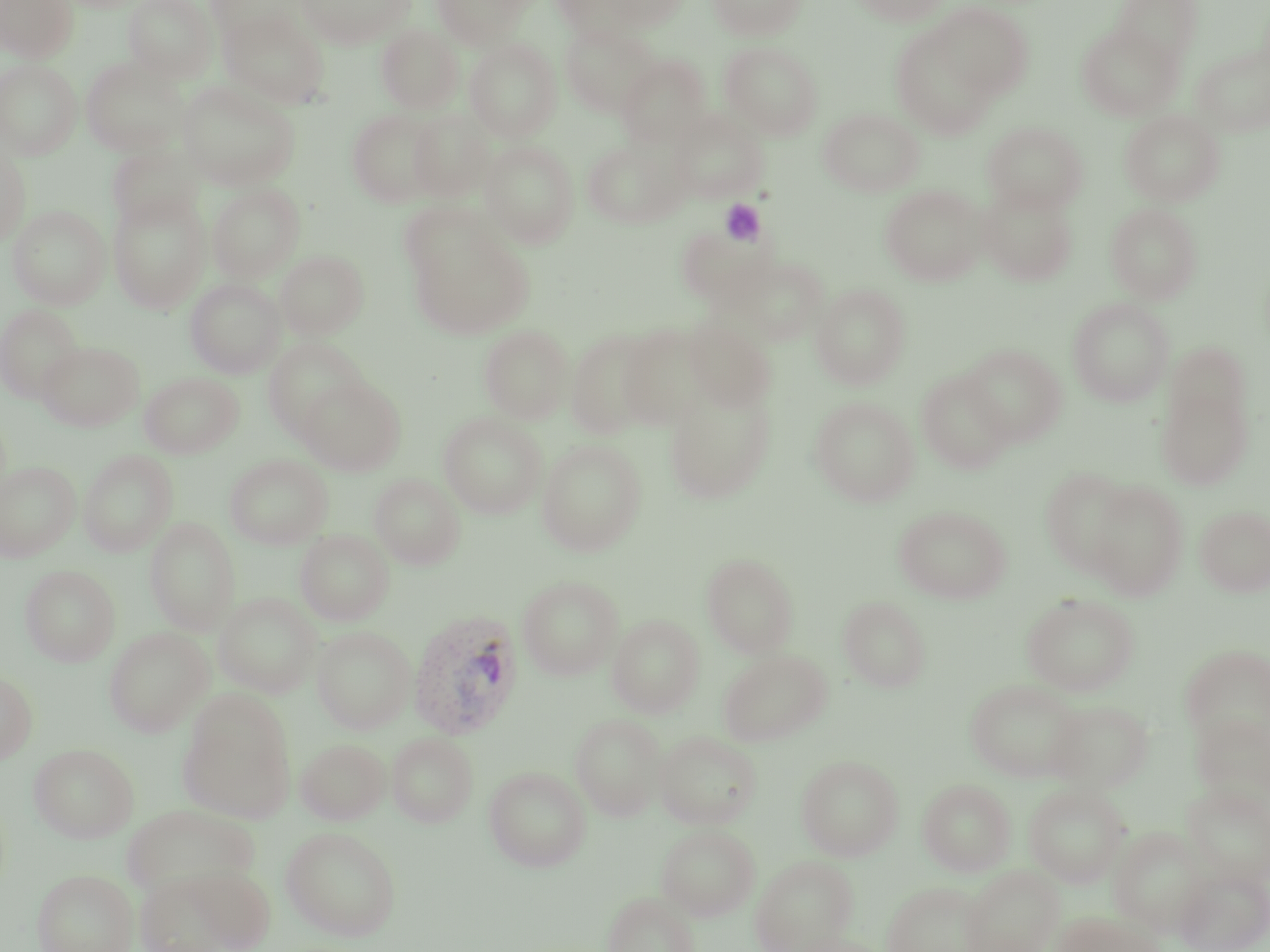
Approximate bounding boxes as [x1, y1, x2, y2] in pixels. Platelet locations: [720, 198, 766, 246]. Uninfected red blood cell locations: [0, 0, 78, 62], [124, 0, 218, 82], [297, 0, 411, 49], [552, 0, 641, 40], [607, 0, 689, 30], [707, 0, 808, 40], [852, 0, 949, 26], [1112, 0, 1202, 68], [206, 1, 306, 46], [430, 1, 530, 47], [931, 2, 1033, 99], [219, 12, 330, 108], [890, 22, 1003, 140], [561, 23, 660, 116], [376, 24, 463, 114], [1076, 24, 1183, 120], [464, 38, 562, 142], [720, 41, 823, 140], [1192, 43, 1270, 138], [617, 55, 710, 147], [81, 57, 188, 156], [0, 58, 82, 159], [177, 80, 300, 190], [819, 108, 923, 197], [346, 109, 443, 207], [1119, 109, 1225, 207], [408, 110, 495, 202], [670, 110, 769, 203], [982, 121, 1088, 214], [582, 138, 685, 228], [480, 140, 579, 248], [106, 143, 204, 232], [0, 147, 31, 246], [207, 183, 305, 283], [880, 184, 987, 285], [977, 184, 1078, 286], [108, 189, 211, 313], [397, 201, 497, 282], [1105, 203, 1202, 303], [8, 205, 111, 309], [410, 230, 532, 339], [275, 249, 369, 339], [735, 256, 829, 344], [185, 278, 285, 378], [811, 284, 911, 389], [1068, 298, 1174, 407], [0, 304, 83, 403], [684, 315, 776, 411], [618, 323, 713, 429], [479, 324, 573, 423], [566, 329, 663, 439], [262, 336, 369, 440], [38, 340, 144, 431], [1164, 341, 1252, 433], [962, 344, 1066, 446], [916, 370, 1015, 474], [140, 372, 243, 458], [297, 374, 406, 475], [663, 382, 776, 504], [1156, 384, 1253, 490], [810, 396, 919, 506], [439, 412, 547, 519], [536, 439, 647, 556], [78, 449, 179, 556], [225, 454, 333, 549], [0, 461, 80, 561], [1040, 467, 1136, 575], [369, 473, 465, 569], [1087, 480, 1188, 599], [894, 505, 1011, 603], [1196, 505, 1270, 596], [145, 517, 240, 635], [295, 529, 394, 625], [701, 552, 800, 657], [20, 564, 120, 666], [518, 575, 623, 680], [214, 592, 322, 698], [1021, 593, 1139, 696], [838, 595, 932, 692], [608, 614, 704, 717], [104, 626, 214, 736], [311, 626, 415, 733], [1181, 644, 1270, 749], [718, 649, 831, 746], [0, 669, 37, 764], [966, 678, 1084, 781], [180, 692, 296, 822], [1044, 699, 1154, 793], [1191, 712, 1269, 809], [569, 713, 667, 820], [654, 730, 762, 829], [387, 733, 478, 827], [296, 738, 390, 825], [29, 742, 139, 843], [796, 754, 903, 860], [484, 766, 591, 871], [918, 778, 1016, 876], [1182, 781, 1270, 887], [1024, 783, 1131, 887], [120, 805, 259, 899], [656, 824, 760, 920], [281, 826, 401, 941], [1109, 827, 1210, 936], [750, 854, 859, 952], [187, 864, 277, 951], [961, 865, 1063, 952], [32, 867, 138, 952], [1174, 867, 1270, 952], [134, 871, 243, 952], [882, 881, 989, 952], [603, 891, 699, 952], [1054, 912, 1161, 952], [784, 934, 891, 952]. Plasmodium vivax-infected red blood cell locations: [409, 609, 525, 740]. Slide-level diagnosis: Plasmodium vivax. Captured at 1000x magnification. Thin blood smear. Single field of view. May-Grünwald-Giemsa-stained preparation. Optical microscopy. Image is 1270×952 pixels.